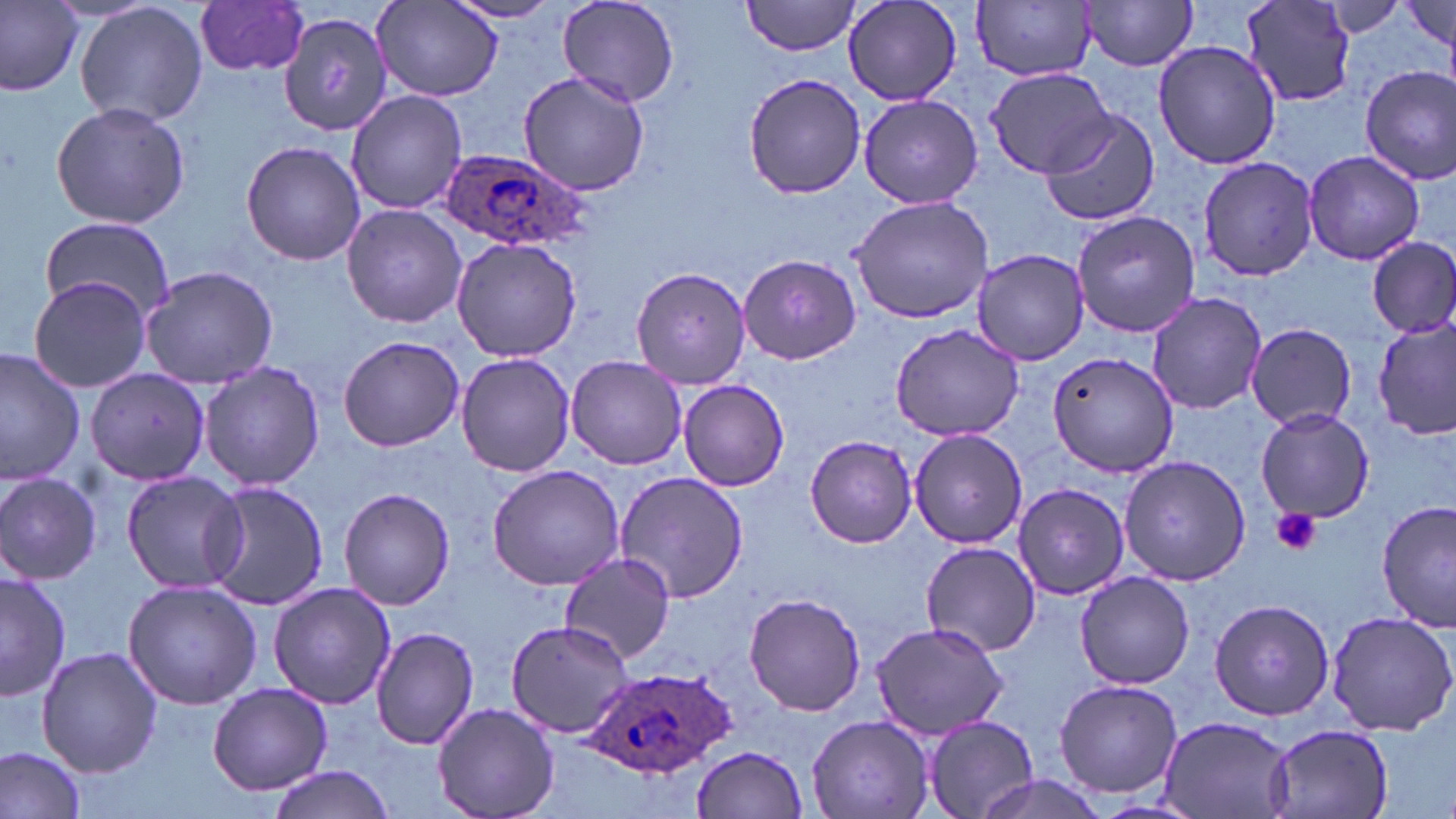
Summary:
  - Coordinate format: approximate bounding boxes as (x1,y1)-(x2,y2) corner pairs in pixels
  - Platelet locations: (1270,507)-(1321,556)
  - Plasmodium ovale-infected red blood cell locations: (435,146)-(588,248), (581,665)-(730,777)
  - Uninfected red blood cell locations: (1,0)-(83,96), (76,0)-(209,127), (443,0)-(566,24), (555,0)-(678,108), (741,0)-(864,56), (843,0)-(963,106), (369,1)-(504,103), (975,1)-(1098,81), (1081,1)-(1201,71), (1312,1)-(1421,37), (194,2)-(312,78), (1237,2)-(1359,108), (1397,2)-(1453,56), (277,18)-(417,156), (1154,40)-(1281,171), (984,66)-(1112,177), (1360,66)-(1456,182), (517,70)-(651,198), (742,72)-(867,200), (346,90)-(469,213), (858,94)-(984,208), (50,101)-(191,229), (1040,108)-(1159,225), (240,140)-(368,266), (1303,149)-(1426,266), (1197,156)-(1321,282), (849,192)-(995,324), (340,205)-(469,329), (1071,208)-(1203,337), (38,219)-(176,321), (451,237)-(583,362), (1368,237)-(1456,339), (971,249)-(1091,365), (738,252)-(860,365), (140,265)-(278,389), (629,266)-(752,389), (28,277)-(153,392), (1146,291)-(1268,415), (1375,317)-(1455,443), (888,321)-(1026,442), (1244,322)-(1357,431), (337,335)-(464,451), (0,348)-(85,486), (1047,351)-(1182,477), (456,353)-(577,478), (567,356)-(688,470), (198,361)-(326,492), (84,367)-(211,486), (679,379)-(790,491), (1255,408)-(1376,523), (908,428)-(1030,548), (804,436)-(916,547), (1119,456)-(1252,586), (487,462)-(627,591), (0,470)-(103,584), (120,470)-(249,594), (617,470)-(749,604), (205,481)-(330,611), (1012,482)-(1131,601), (337,487)-(455,610), (1377,502)-(1455,629), (920,541)-(1040,658), (560,553)-(677,666), (895,557)-(1030,725), (0,569)-(71,702), (1075,572)-(1195,690), (122,580)-(262,709), (268,583)-(397,709), (741,593)-(869,716), (1208,598)-(1334,720), (1325,610)-(1456,737), (504,617)-(636,738), (870,620)-(1009,741), (371,626)-(480,750), (36,646)-(162,777), (1054,678)-(1182,799), (208,683)-(333,794), (432,701)-(560,819), (1157,714)-(1295,819), (806,715)-(933,819), (921,716)-(1040,819), (1264,723)-(1395,819), (0,744)-(87,818), (691,746)-(808,818), (267,766)-(397,819), (967,773)-(1111,819)
  - Slide-level diagnosis: Plasmodium ovale
  - Stain: May-Grünwald-Giemsa
  - Magnification: 1000x
  - Image size: 1456×819 pixels
  - Preparation: thin blood film
  - Field of view: one of a larger specimen
  - Modality: optical microscopy